Identify the parasite.
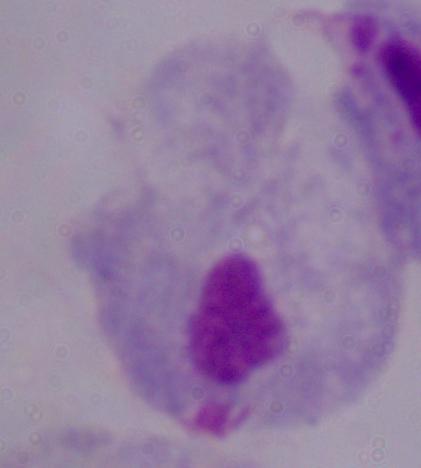
A trichomonad.

Captured at 1000x magnification. Micrograph.